Assess for Plasmodium parasites.
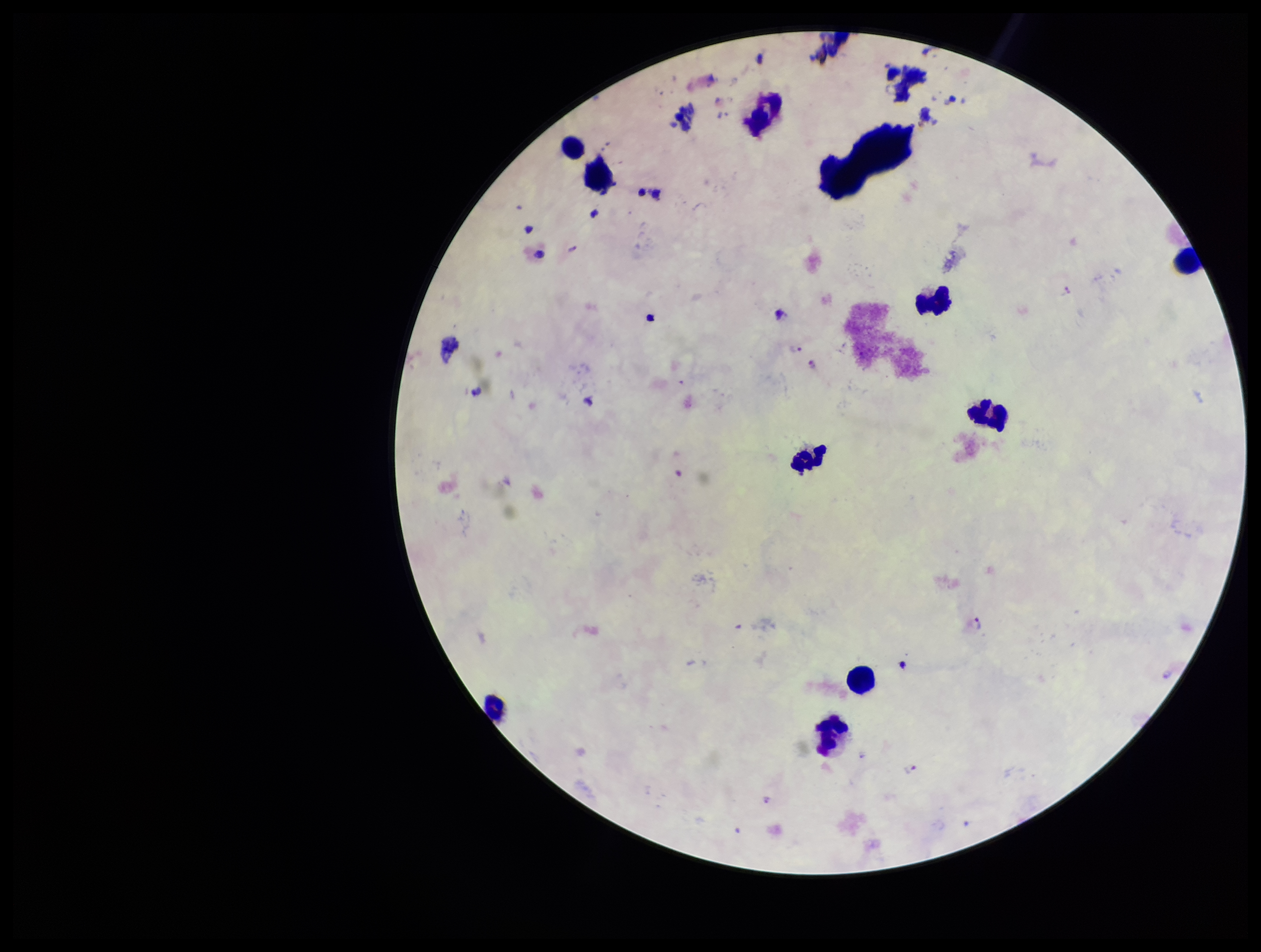
Seen.

leukocyte count = 10
image size = 1261×952 pixels
field of view = one from this slide
patient malaria status = infected
capture = smartphone photograph through the microscope eyepiece
stain = Giemsa
preparation = thick blood smear
species reported for this patient = Plasmodium falciparum
parasite count = 5